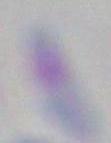

Photomicrograph. Toxoplasma gondii is seen. 1000x magnification.